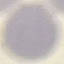

Summary:
  - Result: negative for malaria parasites
  - Stain: Giemsa
  - Image type: automatically extracted cell patch, resized to 64 × 64 pixels
  - Preparation: thin smear
  - Capture: smartphone through the microscope eyepiece